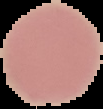

preparation = thin blood film
malaria status = uninfected
image size = 103×109 pixels
image type = segmented cell region with the area outside set to black